Assess this cell for malaria.
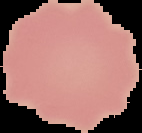

Uninfected.

From a thin blood film. Segmented cell region on a black background. Image is 142×133 pixels.